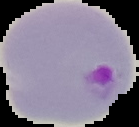
Summary:
  - Image size: 139×127 pixels
  - Image type: segmented cell region with the area outside set to black
  - Preparation: thin blood smear
  - Result: malaria parasites identified